Classify this cell by malaria status.
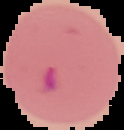

It is parasitized.

Cell region segmented out of the field of view; the surrounding area is masked to black. From a thin blood smear. Image is 124×130 pixels.